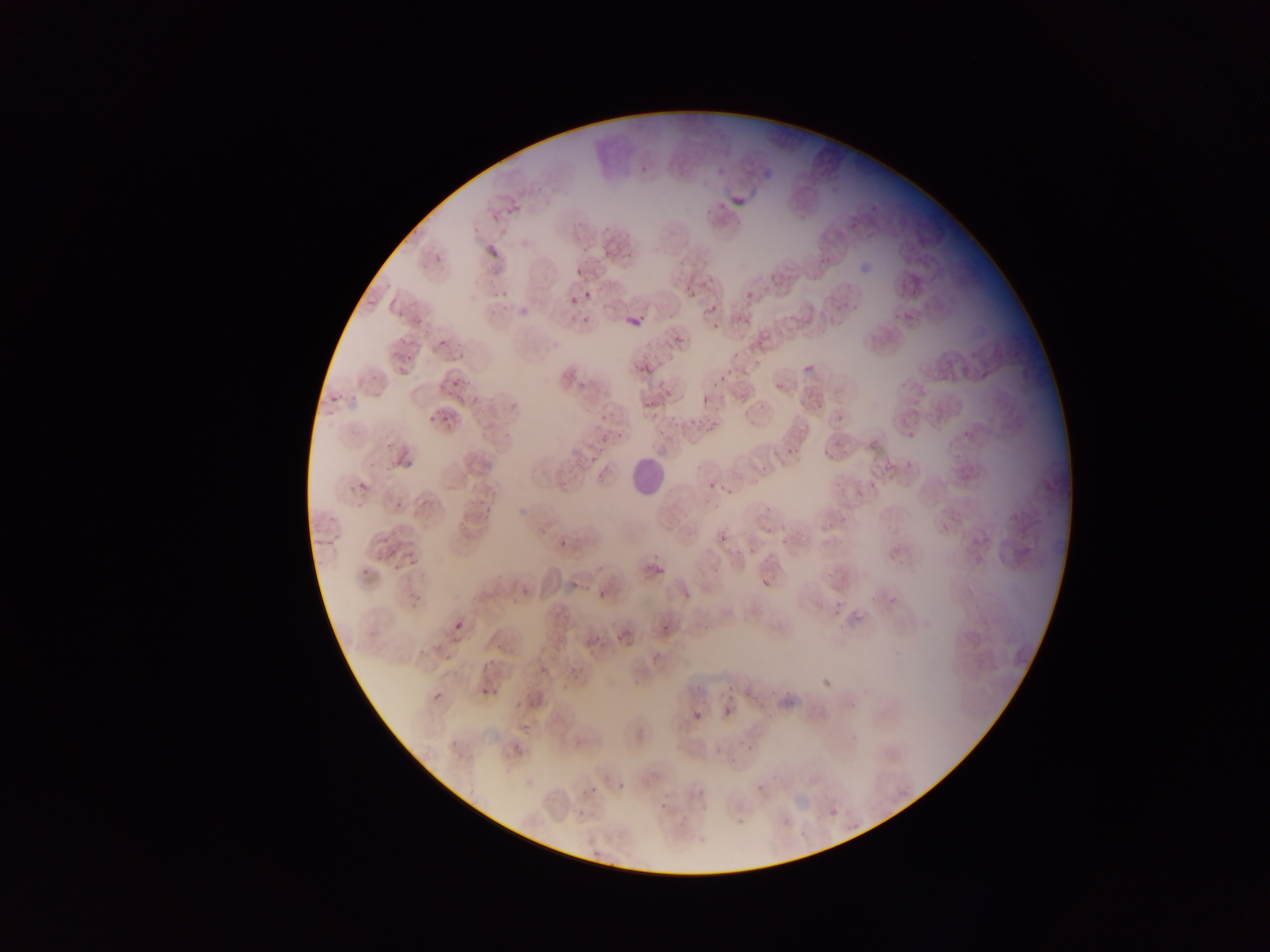
Approximate bounding boxes as left top right bottom in pixels.
Summary:
  - Leukocyte locations: 626 456 665 496
  - Malaria parasite locations: 727 183 767 209; 484 212 505 233; 484 244 501 262; 427 246 452 268; 568 264 581 275; 675 275 697 299; 562 282 586 303; 485 285 508 307; 583 290 592 300; 740 291 753 301; 619 306 641 332; 706 306 718 314; 891 309 917 319; 737 313 753 323; 706 314 729 338; 439 339 449 348; 800 350 818 376; 632 353 673 382; 711 366 741 384; 437 373 479 391; 426 393 468 425; 701 395 709 404; 330 396 337 404; 827 415 848 427; 907 430 916 438; 821 444 844 461; 778 446 797 460; 389 453 414 474; 698 476 721 494; 358 480 368 491; 868 480 875 490; 474 487 499 512; 766 500 788 527; 556 533 579 551; 719 533 728 542; 307 534 342 549; 384 539 396 562; 889 549 906 565; 657 565 664 574; 761 579 770 587; 512 580 531 596; 883 580 907 610; 570 581 580 589; 594 587 604 597; 598 589 606 598; 833 606 842 617; 453 621 462 630; 587 622 614 641; 662 623 670 632; 564 655 590 687; 483 663 492 671; 745 674 763 697; 822 681 833 693; 779 682 797 704; 480 687 491 696; 431 691 442 702; 723 707 732 718; 689 710 705 730; 450 740 458 749; 512 742 521 752; 612 770 631 793; 699 771 722 793; 588 785 598 796; 651 800 663 813; 830 808 838 816; 575 810 584 819; 731 814 749 825; 592 849 600 857
  - Image size: 1270×952 pixels
  - Country: Ghana
  - Field of view: single
  - Capture: mobile-phone photograph through a microscope
  - Preparation: thin blood film